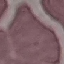

Result: negative for malaria parasites. Giemsa stain. Thin smear of blood. Acquired by smartphone through the microscope eyepiece. Automatically extracted cell patch, resized to 64 × 64 pixels.